Report the malaria status of this cell.
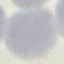
It is uninfected.

stain: Giemsa
capture: smartphone camera at the microscope eyepiece
image_type: cell patch, automatically extracted from a larger field of view and resized to 64 × 64 pixels
preparation: thin smear